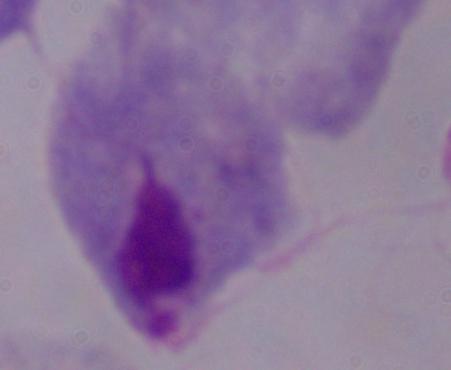

Summary:
  - Identification: trichomonad
  - Modality: photomicrograph
  - Magnification: 1000x